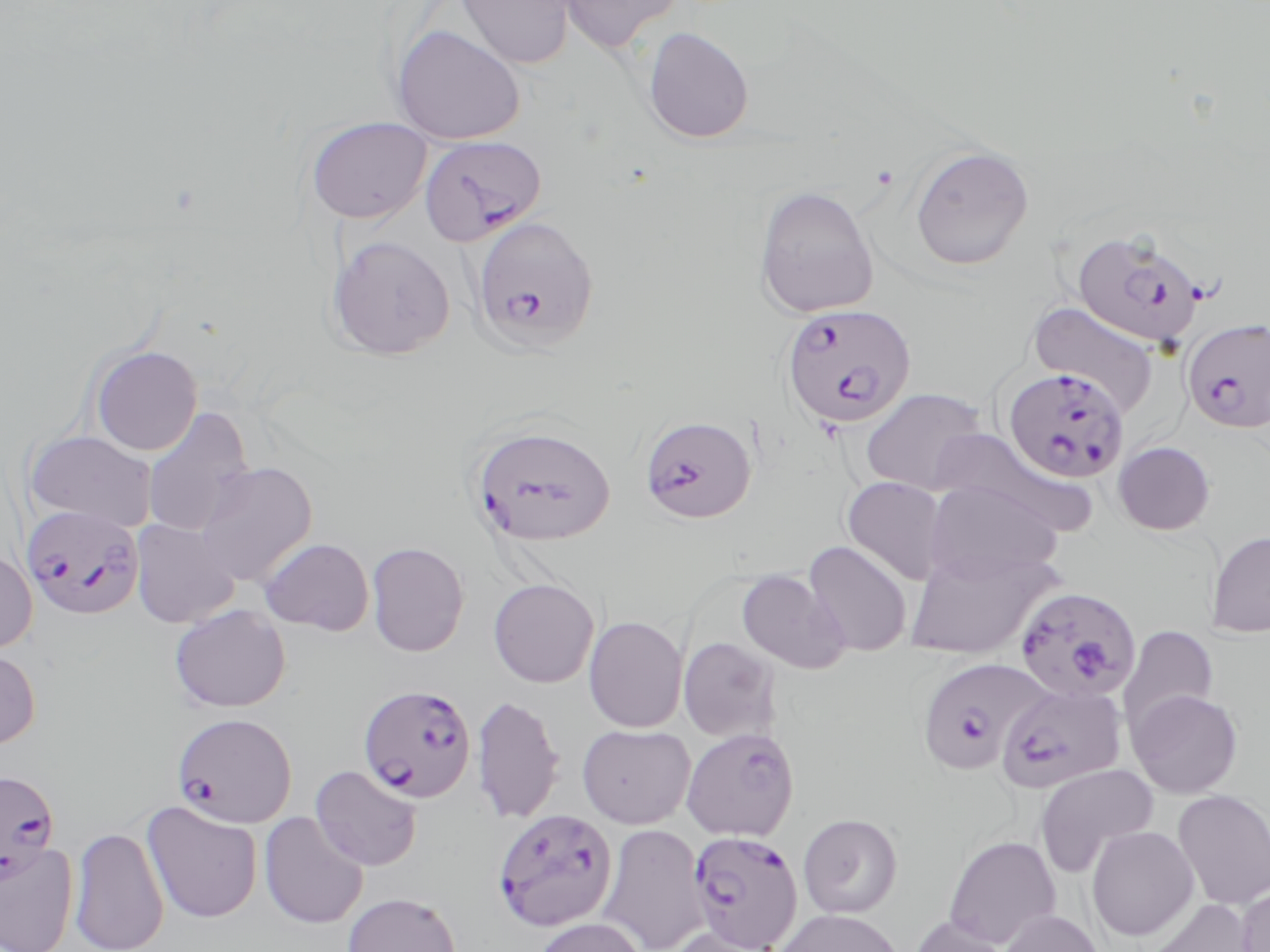

plasmodium_falciparum_infected_red_blood_cell_locations: 'approximate bounding boxes as (x1,y1)-(x2,y2) corner pairs in pixels: (420,135)-(546,246), (470,216)-(599,352), (1072,229)-(1205,349), (780,304)-(916,430), (1182,318)-(1270,433), (1003,368)-(1130,483), (639,414)-(757,523), (470,423)-(616,548), (22,504)-(144,619), (1015,585)-(1148,703), (915,656)-(1048,776), (997,681)-(1127,793), (358,684)-(477,803), (171,712)-(297,828), (680,727)-(799,840), (0,768)-(60,882), (491,809)-(618,932), (687,830)-(803,950)'
slide_level_diagnosis: Plasmodium falciparum
modality: optical microscopy
magnification: 1000x
stain: May-Grünwald-Giemsa
field_of_view: one of a larger specimen
uninfected_red_blood_cell_locations: 'approximate bounding boxes as (x1,y1)-(x2,y2) corner pairs in pixels: (454,0)-(576,70), (557,0)-(684,54), (391,24)-(526,145), (642,26)-(754,144), (305,116)-(432,224), (909,145)-(1034,271), (753,185)-(879,319), (326,234)-(456,360), (1028,301)-(1161,416), (90,345)-(202,455), (859,388)-(989,495), (142,406)-(255,538), (25,431)-(159,532), (1113,441)-(1216,535), (193,461)-(318,587), (842,476)-(949,586), (924,481)-(1063,583), (130,519)-(240,628), (1207,529)-(1270,637), (258,538)-(374,635), (366,541)-(469,657), (803,541)-(912,657), (905,547)-(1056,659), (0,549)-(37,654), (735,568)-(851,674), (488,578)-(599,688), (169,605)-(290,713), (583,616)-(688,733), (1118,624)-(1219,735), (678,637)-(781,742), (0,647)-(40,750), (1128,688)-(1244,799), (471,693)-(565,825), (577,724)-(695,829), (1034,763)-(1159,877), (310,765)-(423,871), (1172,789)-(1270,911), (142,801)-(262,924), (259,812)-(369,930), (798,813)-(902,918), (596,824)-(711,952), (69,826)-(169,951), (1086,826)-(1198,941), (943,834)-(1062,949), (0,841)-(79,952), (1236,884)-(1270,952), (342,892)-(462,952), (1140,897)-(1257,952), (774,908)-(904,952), (999,909)-(1105,952), (908,916)-(1012,952), (535,917)-(645,952), (669,924)-(784,951)'
image_size: 1270×952 pixels
preparation: thin blood film